Report the malaria status of this cell.
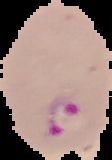
Parasitized.

Summary:
  - Image type: segmented cell region with the area outside set to black
  - Preparation: thin blood film
  - Image size: 112×160 pixels